Report the malaria status of this cell.
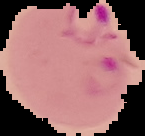

It is parasitized.

preparation = thin blood smear
image size = 145×136 pixels
image type = segmented cell region on a black background